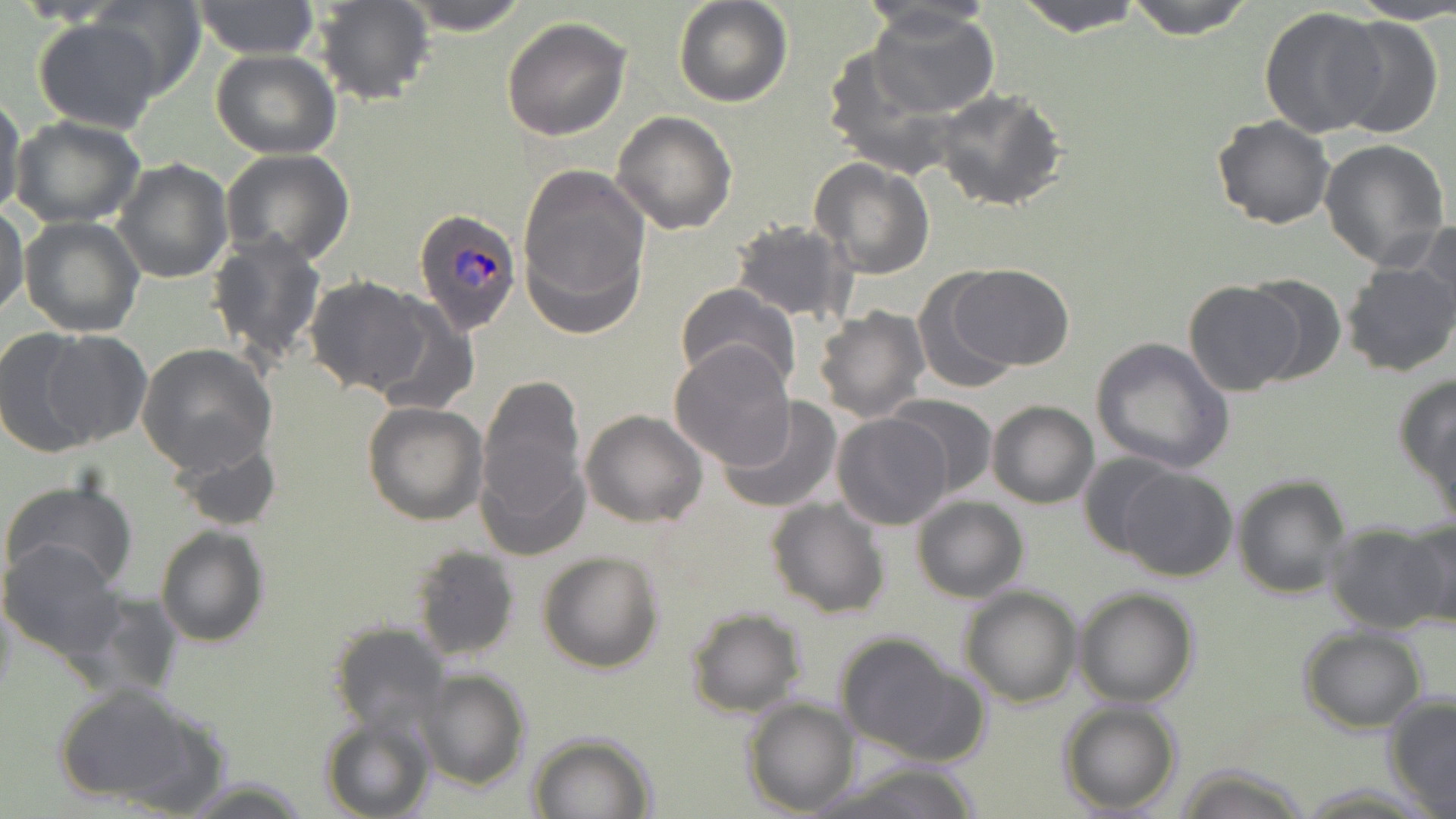 Approximate bounding boxes as [x1, y1, x2, y2] in pixels. Plasmodium ovale-infected red blood cell locations: [413, 208, 523, 335]. Uninfected red blood cell locations: [398, 0, 532, 34], [673, 0, 793, 108], [856, 0, 996, 38], [1015, 0, 1146, 34], [1123, 0, 1257, 38], [1341, 0, 1456, 24], [193, 1, 320, 59], [312, 1, 434, 106], [90, 2, 205, 99], [1258, 6, 1387, 139], [868, 9, 999, 117], [500, 15, 631, 139], [1331, 15, 1443, 140], [31, 18, 166, 132], [818, 44, 959, 175], [211, 49, 340, 160], [932, 90, 1068, 211], [0, 94, 26, 223], [612, 111, 738, 236], [1212, 114, 1335, 230], [11, 116, 145, 226], [1319, 138, 1451, 271], [220, 148, 356, 266], [113, 158, 232, 284], [809, 158, 935, 278], [517, 164, 651, 334], [0, 201, 29, 319], [20, 216, 144, 336], [727, 219, 853, 325], [1413, 220, 1455, 334], [1388, 231, 1456, 358], [208, 232, 327, 367], [1340, 263, 1456, 377], [947, 264, 1075, 370], [913, 272, 1023, 396], [303, 275, 433, 395], [1244, 275, 1346, 385], [674, 282, 800, 391], [1183, 282, 1305, 396], [368, 298, 478, 412], [813, 307, 928, 424], [0, 329, 102, 456], [41, 330, 150, 447], [1090, 337, 1234, 473], [668, 339, 797, 469], [137, 344, 277, 474], [1394, 372, 1456, 497], [475, 389, 588, 550], [884, 395, 998, 497], [718, 398, 841, 515], [362, 400, 488, 524], [986, 400, 1099, 508], [580, 410, 709, 528], [1428, 411, 1456, 533], [833, 413, 954, 530], [167, 434, 283, 533], [1080, 453, 1180, 558], [1116, 467, 1238, 582], [1231, 474, 1352, 599], [3, 476, 137, 592], [911, 495, 1028, 603], [765, 496, 891, 621], [1400, 517, 1456, 629], [1324, 523, 1448, 634], [155, 525, 269, 647], [0, 539, 126, 660], [411, 545, 520, 661], [537, 550, 665, 674], [959, 585, 1082, 708], [1073, 587, 1200, 707], [684, 607, 806, 717], [327, 622, 448, 735], [1299, 624, 1428, 732], [833, 631, 981, 764], [416, 670, 530, 791], [50, 682, 216, 809], [1383, 693, 1456, 815], [742, 699, 859, 815], [1058, 700, 1182, 815], [319, 714, 435, 819], [528, 732, 657, 818], [820, 761, 987, 818], [1172, 763, 1311, 819], [181, 778, 310, 816]. Slide-level diagnosis: Plasmodium ovale. Optical microscopy. Thin blood smear. May-Grünwald-Giemsa-stained preparation. Image is 1456×819 pixels. Single field of view. 1000x magnification.